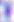
identification = Toxoplasma gondii
modality = photomicrograph
magnification = 400x